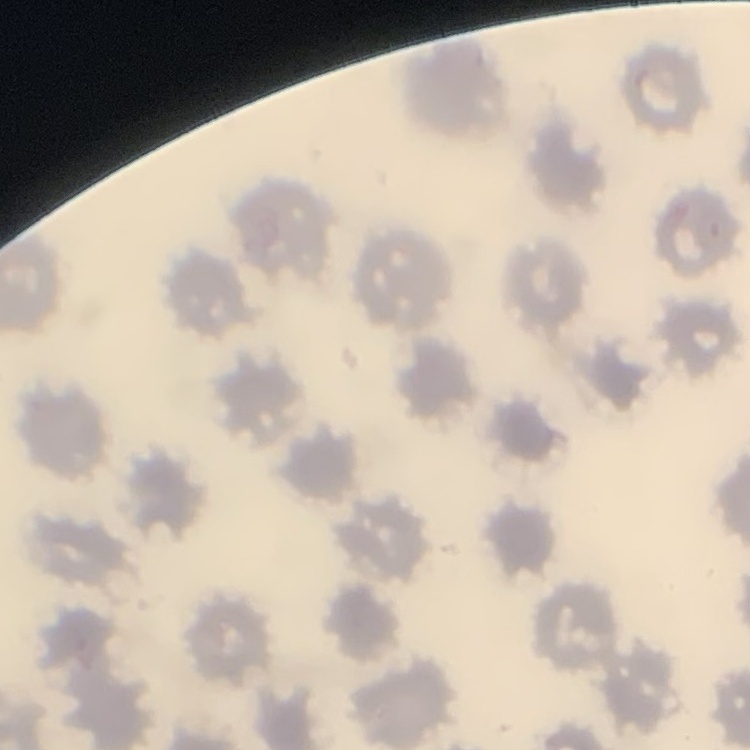 The red blood cells exhibit no rouleaux formation. Square crop of a larger photomicrograph. Field's or Giemsa stain. Thin blood film.